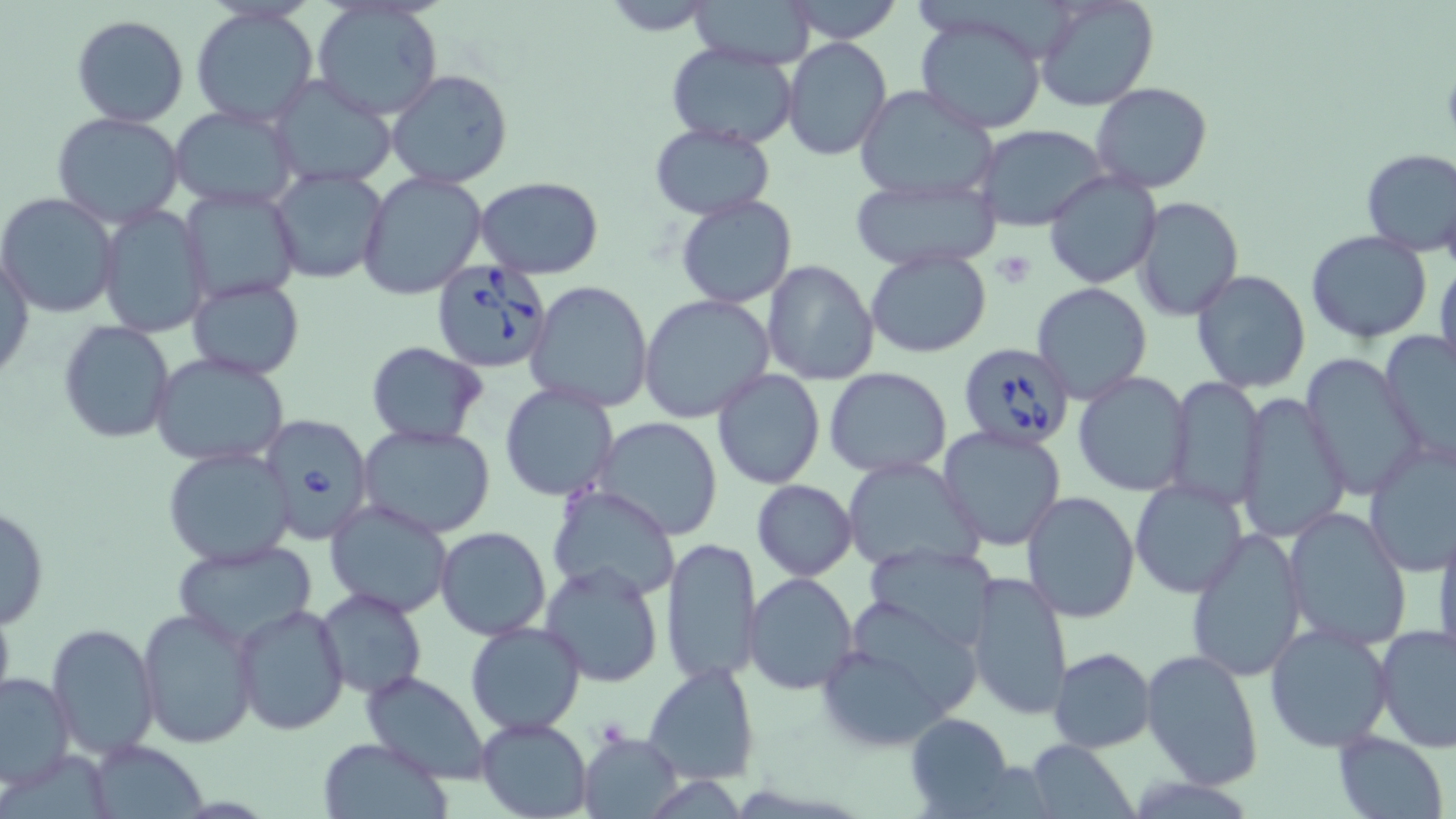

Summary:
  - Coordinate format: approximate bounding boxes as [x1, y1, x2, y2] in pixels
  - Babesia divergens-infected red blood cell locations: [429, 261, 554, 376], [956, 340, 1075, 451], [257, 413, 373, 544]
  - Platelet locations: [992, 250, 1037, 288], [595, 715, 632, 750]
  - Uninfected red blood cell locations: [602, 0, 720, 34], [687, 0, 818, 69], [785, 0, 904, 44], [1035, 0, 1159, 112], [312, 5, 442, 120], [190, 6, 319, 128], [913, 12, 1049, 134], [71, 15, 190, 128], [782, 37, 892, 160], [664, 42, 800, 150], [387, 67, 513, 190], [269, 75, 398, 189], [1092, 82, 1213, 194], [855, 85, 998, 202], [171, 106, 298, 210], [51, 111, 187, 227], [650, 124, 776, 220], [973, 124, 1109, 230], [1359, 147, 1456, 258], [269, 169, 388, 284], [1044, 170, 1162, 290], [359, 173, 487, 300], [848, 176, 1000, 271], [475, 177, 603, 277], [180, 185, 304, 308], [0, 193, 121, 319], [676, 196, 797, 308], [1133, 198, 1243, 320], [97, 205, 209, 337], [1306, 230, 1434, 344], [865, 246, 991, 357], [1, 247, 34, 385], [1434, 257, 1456, 378], [762, 260, 881, 385], [1191, 268, 1311, 393], [188, 278, 304, 381], [526, 280, 654, 412], [1032, 282, 1151, 404], [639, 295, 774, 426], [59, 320, 175, 442], [1380, 329, 1456, 467], [365, 342, 487, 446], [1302, 352, 1423, 501], [151, 353, 290, 467], [825, 367, 951, 478], [712, 368, 824, 491], [1074, 371, 1193, 496], [1165, 376, 1264, 508], [499, 383, 617, 501], [1237, 391, 1349, 542], [595, 416, 724, 539], [357, 423, 496, 539], [937, 426, 1067, 551], [1364, 439, 1456, 576], [163, 446, 296, 566], [841, 456, 985, 573], [1130, 477, 1250, 600], [752, 479, 858, 581], [546, 483, 681, 603], [1022, 491, 1139, 623], [324, 498, 454, 618], [0, 503, 49, 629], [1285, 507, 1413, 650], [1432, 517, 1456, 665], [1186, 526, 1307, 682], [435, 527, 552, 641], [660, 536, 761, 686], [169, 541, 318, 647], [865, 543, 1000, 654], [540, 559, 667, 687], [964, 569, 1073, 721], [744, 572, 858, 695], [315, 586, 427, 699], [231, 602, 349, 736], [855, 603, 983, 714], [136, 606, 259, 748], [46, 621, 161, 758], [464, 621, 587, 736], [1264, 621, 1396, 754], [814, 623, 974, 751], [1375, 623, 1456, 752], [1048, 647, 1156, 751], [1140, 647, 1265, 791], [643, 660, 759, 785], [360, 671, 492, 783], [0, 672, 74, 788], [906, 713, 1013, 817], [476, 717, 592, 819], [1333, 730, 1450, 819], [580, 733, 683, 818], [318, 736, 450, 817], [82, 739, 212, 818], [1027, 740, 1138, 819]
  - Slide-level diagnosis: Babesia divergens
  - Magnification: 1000x
  - Field of view: one of a larger specimen
  - Stain: May-Grünwald-Giemsa
  - Modality: light microscopy
  - Preparation: thin blood film
  - Image size: 1456×819 pixels